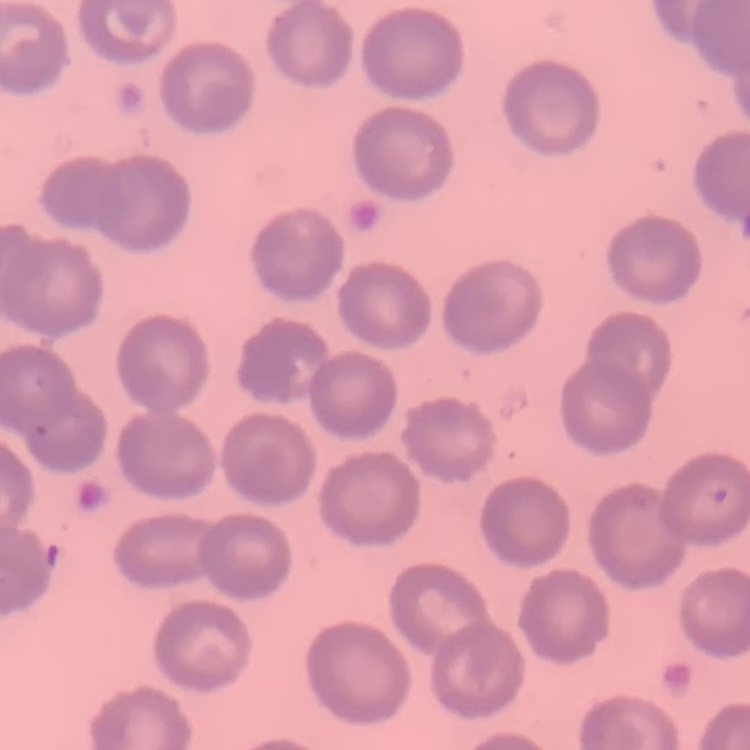
The red blood cells show no rouleaux formation. Thin peripheral smear. Field's or Giemsa stain. One tile cut from a larger photomicrograph.